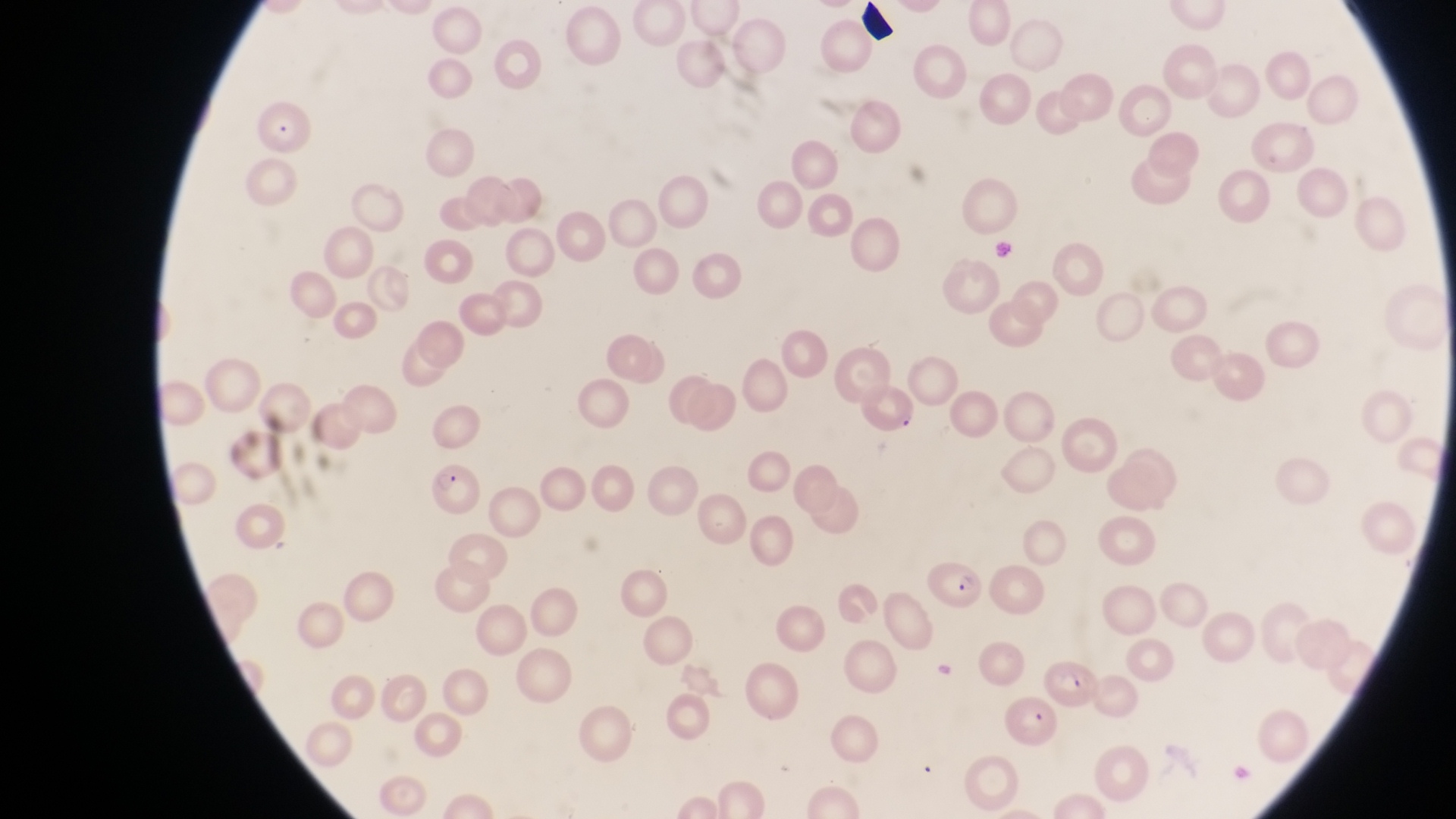
Approximate bounding boxes as [left, top, right, bottom] in pixels.
Summary:
  - Parasitised red blood cell locations: [859, 381, 923, 440], [423, 465, 481, 523], [925, 555, 988, 614], [1046, 657, 1099, 710], [999, 692, 1060, 747]
  - Artifact (platelet-like body, stain precipitate, or debris) locations: [858, 0, 899, 46], [264, 121, 291, 142]
  - Field of view: single
  - Country: Uganda
  - Image size: 1456×819 pixels
  - Capture: smartphone photograph through the eyepiece of an Olympus CX-23 microscope
  - Preparation: thin blood smear
  - Magnification: 1000x